Report the malaria status of this cell.
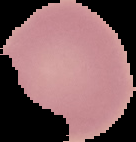

Uninfected.

Cell region segmented out of the field of view; the surrounding area is masked to black. From a thin blood smear. Image is 136×142 pixels.